Classify this cell by malaria status.
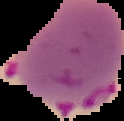

It is parasitized.

Segmented cell region on a black background. Image is 124×121 pixels. From a thin blood film.